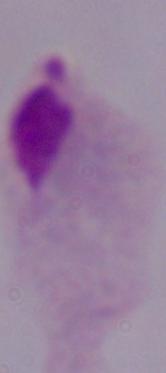 Photomicrograph. Captured at 1000x magnification. A trichomonad is seen.